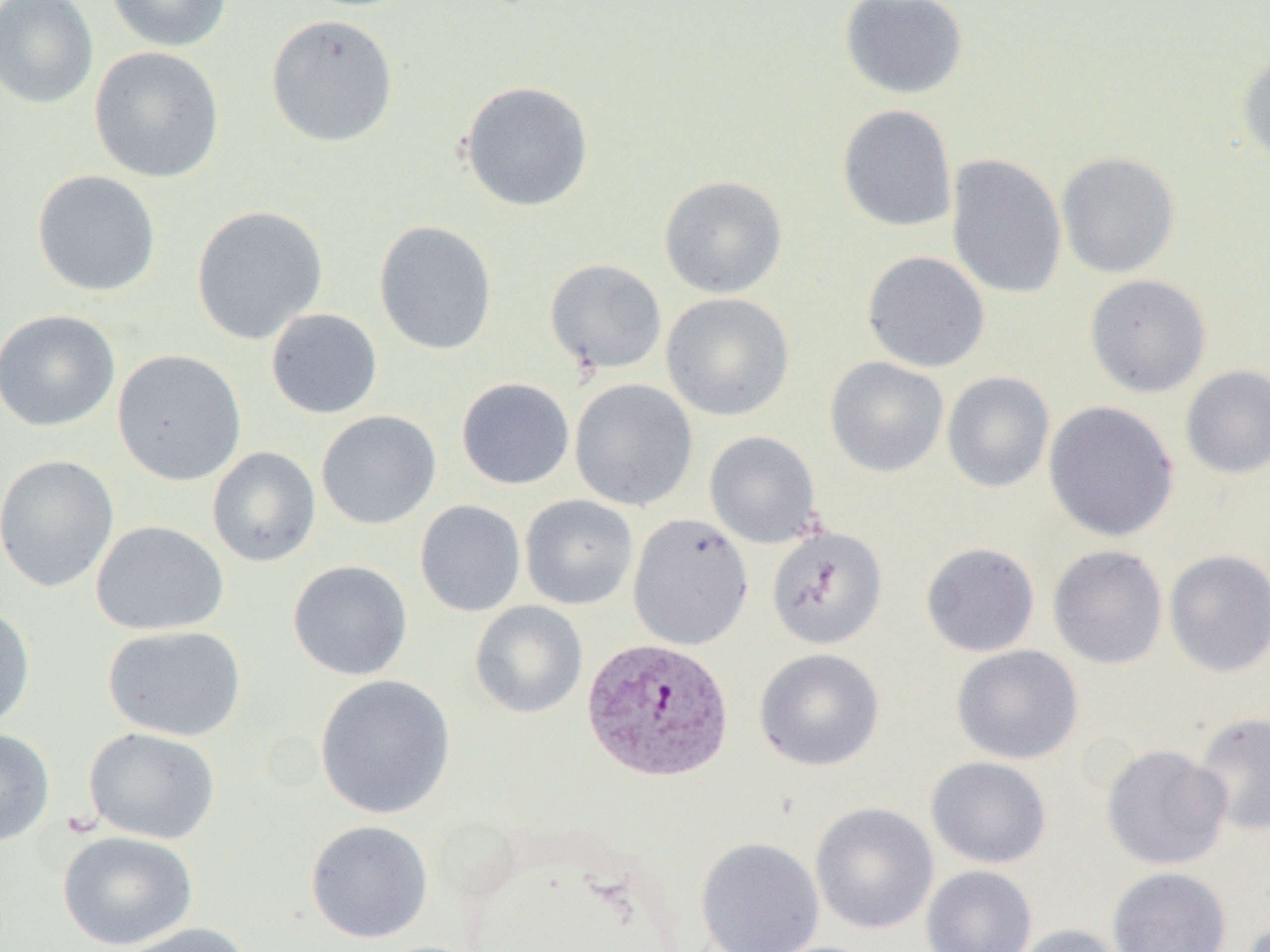
Approximate bounding boxes as (x1, y1, x2, y2) in pixels. Uninfected red blood cell locations: (0, 0, 99, 109), (106, 0, 232, 52), (839, 0, 969, 101), (266, 14, 399, 147), (88, 46, 225, 184), (1237, 51, 1270, 165), (459, 80, 595, 213), (837, 104, 957, 233), (1056, 151, 1180, 279), (946, 153, 1067, 299), (32, 170, 161, 297), (659, 175, 788, 299), (191, 205, 328, 345), (374, 220, 497, 356), (861, 250, 990, 373), (544, 258, 668, 374), (1083, 274, 1212, 398), (661, 293, 795, 421), (265, 307, 383, 419), (0, 310, 121, 431), (111, 349, 248, 486), (825, 356, 949, 477), (1180, 365, 1270, 479), (942, 371, 1055, 493), (456, 378, 575, 490), (569, 378, 699, 511), (1043, 400, 1179, 542), (316, 410, 442, 530), (704, 431, 823, 550), (207, 446, 322, 567), (0, 454, 120, 593), (519, 494, 638, 610), (415, 500, 526, 617), (627, 513, 754, 651), (91, 520, 229, 636), (766, 526, 888, 650), (921, 542, 1040, 657), (1048, 545, 1168, 669), (1164, 550, 1270, 677), (288, 559, 413, 680), (469, 600, 588, 719), (0, 605, 35, 731), (102, 625, 246, 741), (951, 644, 1083, 764), (754, 648, 885, 770), (314, 674, 457, 820), (1192, 712, 1270, 836), (83, 726, 222, 844), (0, 728, 55, 848), (1101, 744, 1232, 870), (926, 756, 1052, 868), (809, 802, 939, 935), (304, 819, 435, 944), (57, 830, 199, 950), (695, 836, 825, 952), (921, 864, 1038, 952), (1108, 867, 1232, 952), (113, 921, 256, 952), (1009, 924, 1127, 952). Plasmodium vivax-infected red blood cell locations: (581, 637, 734, 782). Slide-level diagnosis: Plasmodium vivax. Thin blood film. Optical microscopy. Single field of view. Image is 1270×952 pixels. 1000x magnification.